Classify this cell by malaria status.
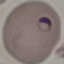
Parasitized.

Photographed with a smartphone camera at the microscope eyepiece. Thin smear of blood. Giemsa stain. Automatically extracted cell patch, resized to 64 × 64 pixels.